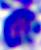 400x magnification. Micrograph. A leukocyte is shown.